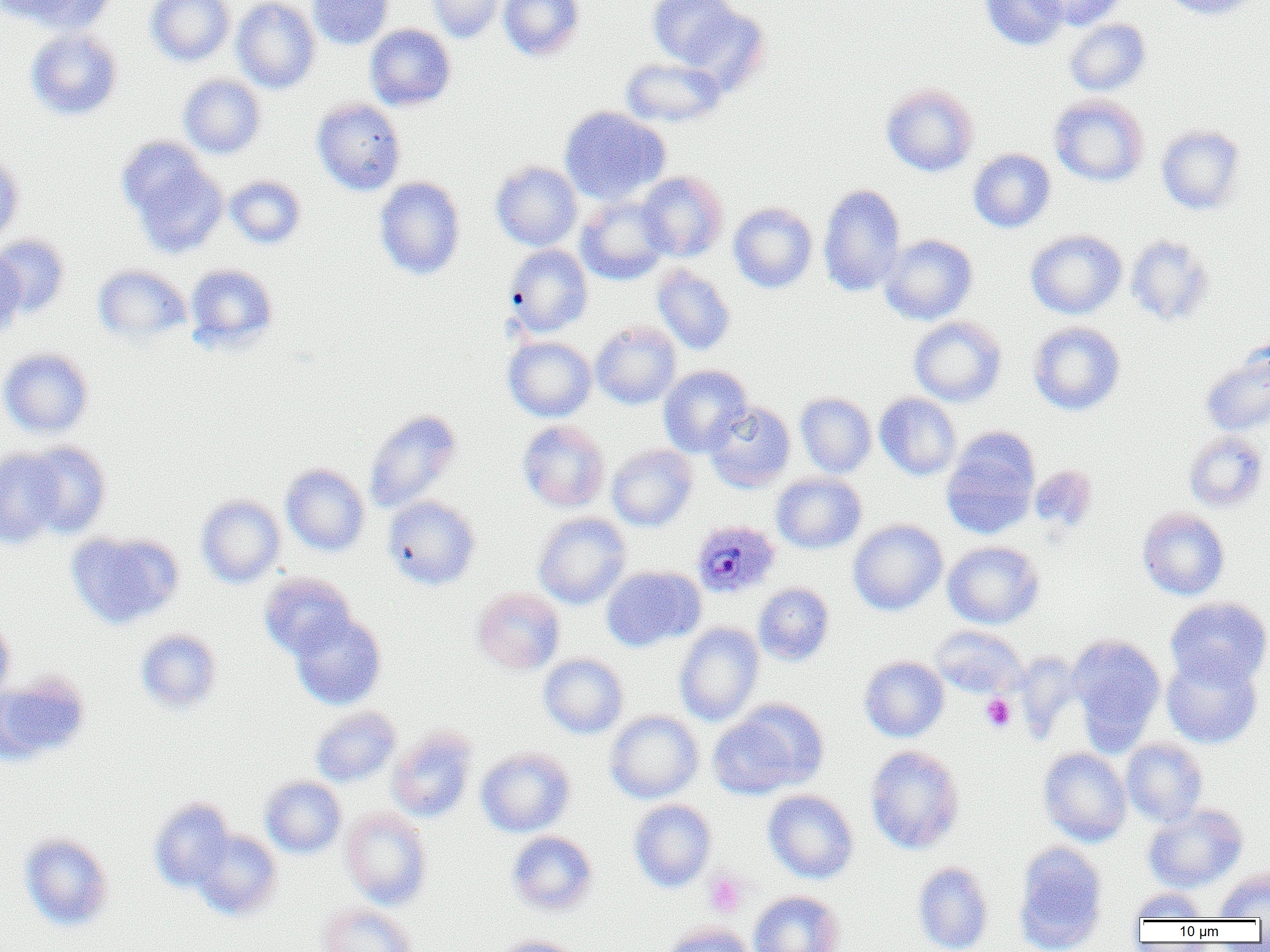

Summary:
  - Coordinate format: approximate bounding boxes as [x1, y1, x2, y2] in pixels
  - Plasmodium ovale-infected red blood cell locations: [692, 520, 781, 600]
  - Uninfected red blood cell locations: [6, 0, 117, 35], [145, 0, 235, 67], [232, 0, 320, 94], [307, 0, 394, 50], [426, 0, 506, 43], [498, 0, 584, 61], [647, 0, 748, 73], [979, 0, 1069, 51], [1032, 0, 1127, 30], [1158, 0, 1260, 20], [1063, 19, 1151, 96], [364, 24, 456, 111], [24, 28, 123, 121], [620, 58, 726, 128], [178, 74, 267, 159], [881, 83, 979, 177], [1048, 93, 1149, 187], [311, 98, 406, 195], [559, 106, 670, 205], [1156, 124, 1246, 215], [115, 136, 228, 258], [968, 149, 1056, 233], [0, 151, 24, 250], [491, 161, 583, 251], [635, 170, 729, 262], [224, 174, 307, 249], [374, 177, 466, 280], [818, 183, 906, 297], [576, 195, 671, 285], [728, 202, 817, 293], [1025, 229, 1127, 319], [880, 233, 978, 325], [1, 234, 70, 318], [1124, 234, 1216, 327], [504, 244, 593, 338], [0, 246, 26, 339], [185, 263, 279, 353], [92, 264, 192, 345], [652, 265, 736, 356], [909, 316, 1007, 407], [590, 321, 681, 409], [1028, 321, 1125, 416], [503, 336, 597, 422], [1200, 345, 1270, 437], [0, 347, 94, 438], [658, 365, 753, 457], [795, 393, 876, 478], [875, 393, 961, 481], [704, 402, 796, 492], [364, 409, 462, 513], [517, 419, 610, 512], [941, 429, 1041, 540], [1183, 430, 1269, 513], [22, 441, 112, 538], [607, 444, 697, 531], [0, 448, 66, 548], [280, 463, 370, 556], [1029, 466, 1097, 533], [771, 473, 867, 554], [195, 494, 286, 589], [382, 495, 481, 590], [1137, 507, 1230, 600], [534, 512, 631, 609], [848, 519, 948, 616], [66, 530, 183, 629], [942, 540, 1045, 629], [600, 565, 704, 651], [259, 572, 356, 659], [753, 583, 835, 666], [473, 587, 565, 674], [1165, 597, 1270, 689], [288, 611, 386, 710], [0, 612, 16, 707], [674, 622, 764, 726], [931, 625, 1028, 698], [135, 628, 224, 715], [1066, 634, 1166, 752], [538, 653, 629, 739], [1161, 653, 1263, 749], [859, 656, 949, 742], [0, 673, 90, 767], [708, 703, 823, 799], [310, 706, 401, 787], [604, 710, 704, 803], [387, 728, 477, 823], [1121, 738, 1208, 826], [864, 745, 965, 854], [476, 747, 576, 837], [1037, 747, 1132, 846], [260, 776, 347, 858], [762, 789, 860, 884], [149, 799, 235, 892], [628, 799, 717, 893], [1143, 803, 1248, 893], [340, 807, 432, 909], [190, 829, 283, 920], [506, 831, 599, 916], [18, 832, 114, 932], [1013, 843, 1109, 952], [912, 861, 994, 952], [1213, 865, 1270, 920], [1128, 888, 1210, 922], [748, 890, 845, 952], [317, 902, 419, 952], [662, 922, 755, 952], [492, 935, 586, 952]
  - Platelet locations: [980, 694, 1016, 732], [704, 870, 749, 918]
  - Slide-level diagnosis: Plasmodium ovale
  - Modality: optical microscopy
  - Field of view: one of a larger specimen
  - Preparation: thin blood film
  - Image size: 1270×952 pixels
  - Magnification: 1000x